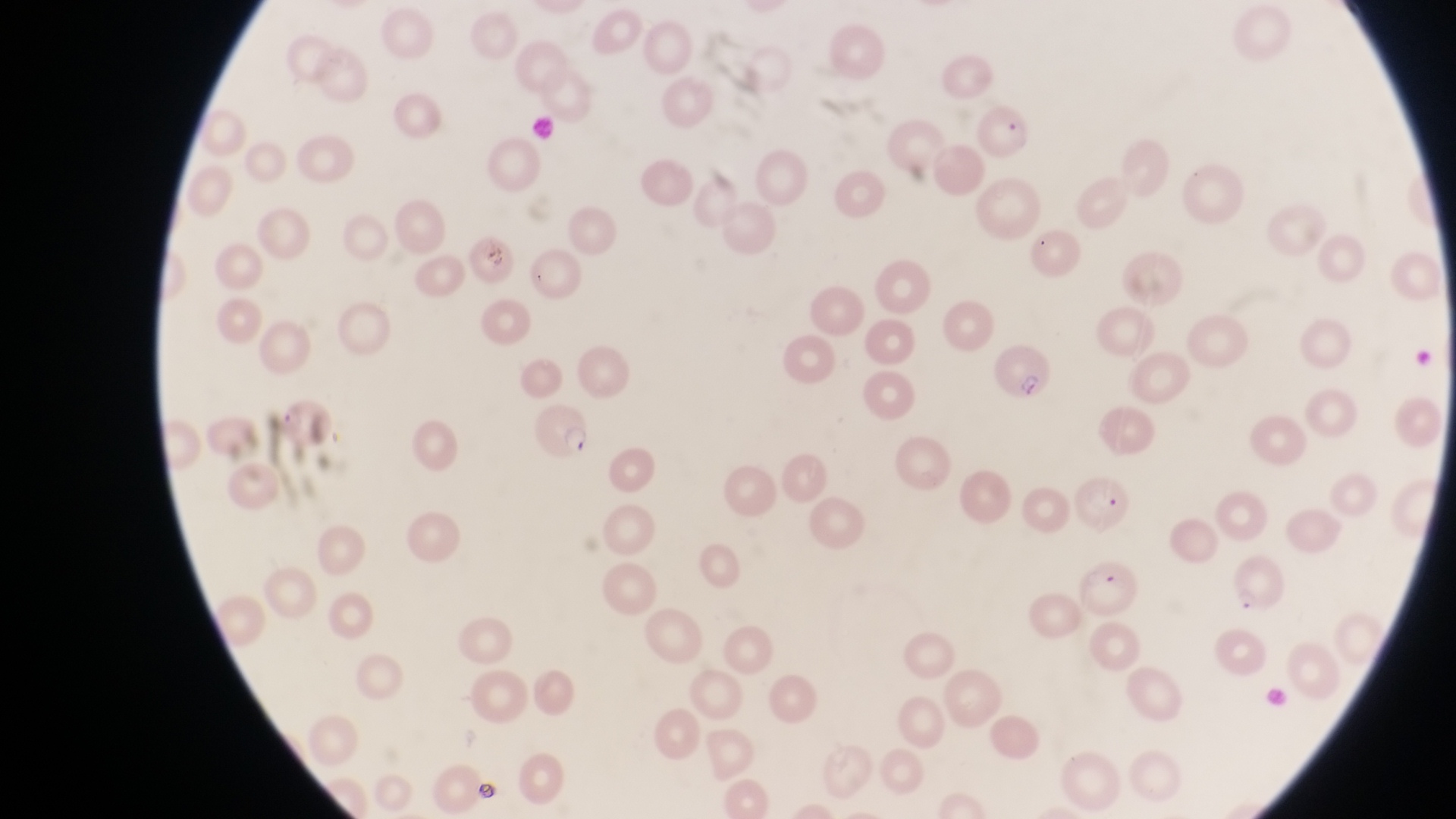

Approximate bounding boxes as [left, top, right, bottom] in pixels.
Summary:
  - Parasitised red blood cell locations: [991, 341, 1054, 405], [532, 407, 596, 466], [1075, 476, 1133, 534], [1075, 554, 1142, 618]
  - Artifact (platelet-like body, stain precipitate, or debris) locations: [478, 237, 511, 269], [470, 779, 496, 803]
  - Capture: smartphone photograph through the eyepiece of an Olympus CX-23 microscope
  - Field of view: single
  - Preparation: thin blood smear
  - Magnification: 1000x
  - Country: Uganda
  - Image size: 1456×819 pixels